Name the blood parasite species.
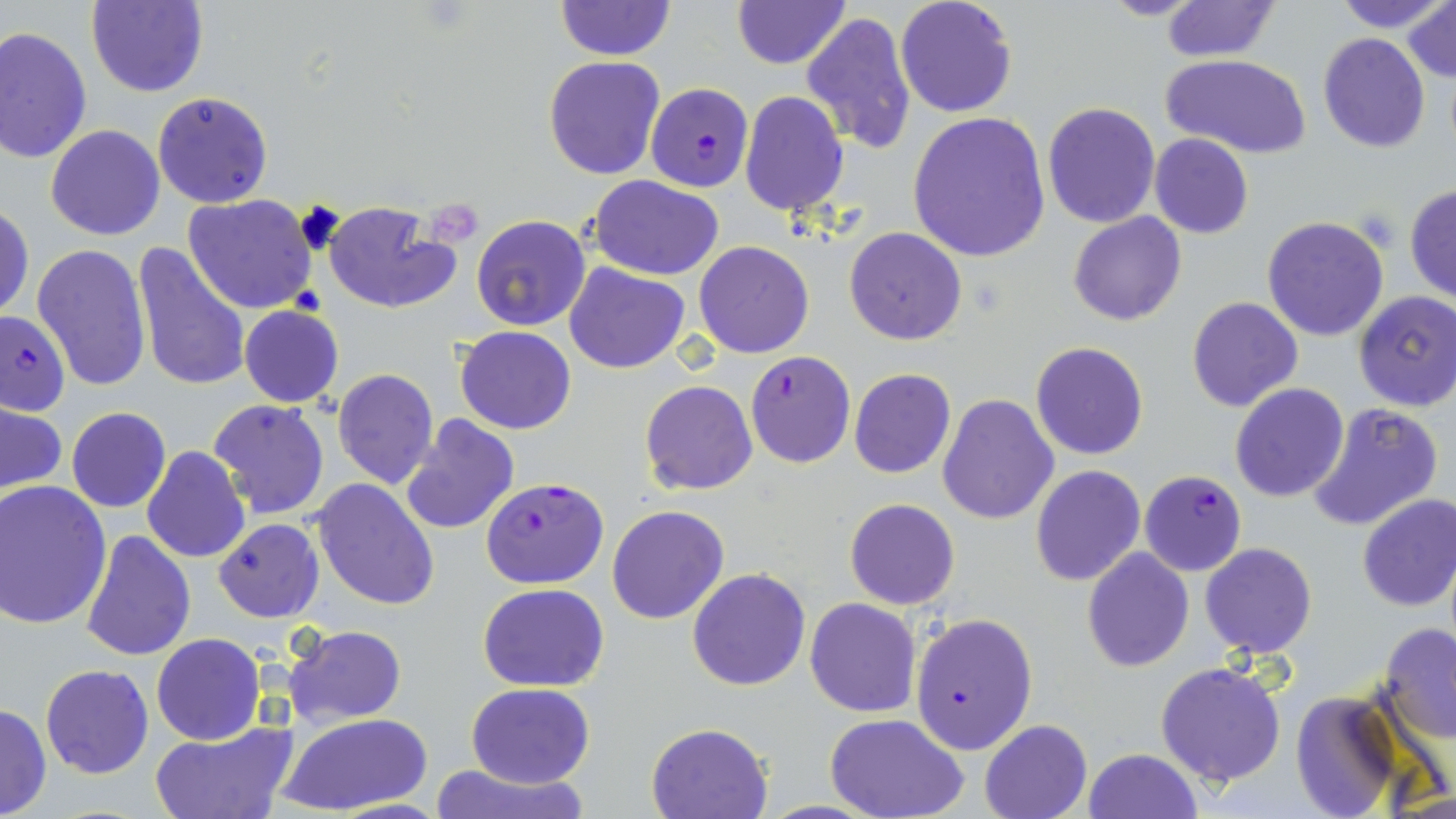
Plasmodium falciparum.

Approximate bounding boxes as (x1,y1)-(x2,y2) corner pairs in pixels. Uninfected red blood cell locations: (86,0)-(209,98), (554,0)-(675,60), (895,0)-(1017,118), (1097,0)-(1206,21), (1162,0)-(1281,61), (1333,0)-(1449,32), (732,1)-(850,70), (1404,3)-(1456,82), (801,11)-(916,154), (0,26)-(93,163), (1318,32)-(1430,151), (1161,53)-(1313,159), (543,56)-(665,179), (152,90)-(274,208), (739,91)-(849,215), (1042,101)-(1161,228), (908,112)-(1051,261), (46,125)-(164,241), (1151,134)-(1254,238), (588,175)-(725,281), (1404,184)-(1456,305), (183,194)-(319,314), (1,200)-(34,323), (323,201)-(462,313), (1068,212)-(1187,326), (471,215)-(592,331), (1261,215)-(1389,341), (844,227)-(968,346), (130,241)-(250,393), (694,241)-(814,358), (32,243)-(151,393), (564,263)-(691,374), (1354,291)-(1456,412), (1186,297)-(1304,413), (238,304)-(344,408), (455,325)-(577,435), (1030,342)-(1148,460), (332,369)-(439,490), (849,369)-(957,479), (640,380)-(758,495), (1228,382)-(1349,503), (936,393)-(1059,525), (208,398)-(330,521), (1306,401)-(1443,533), (1,403)-(67,498), (66,408)-(171,513), (399,415)-(521,537), (141,446)-(250,564), (1029,465)-(1145,586), (309,477)-(440,611), (0,481)-(112,630), (1356,494)-(1456,612), (845,498)-(960,610), (608,504)-(729,624), (214,519)-(324,622), (80,530)-(196,663), (1199,543)-(1318,657), (1081,549)-(1194,673), (687,568)-(810,691), (478,583)-(610,692), (805,597)-(922,718), (1378,622)-(1456,743), (282,624)-(407,728), (152,633)-(266,744), (1156,661)-(1287,787), (40,664)-(154,779), (466,681)-(594,787), (1290,688)-(1409,819), (0,703)-(51,819), (277,713)-(430,817), (826,714)-(970,819), (978,719)-(1092,819), (149,720)-(299,819), (647,723)-(771,818), (1083,747)-(1201,819), (425,763)-(589,819). Plasmodium falciparum-infected red blood cell locations: (645,83)-(754,192), (0,308)-(69,418), (745,350)-(855,467), (1139,470)-(1248,576), (480,476)-(608,589), (908,612)-(1038,757). Thin blood smear. Image is 1456×819 pixels. Captured at 1000x magnification. Single field of view. Optical microscopy. May-Grünwald-Giemsa-stained preparation.